Assess the morphology of the erythrocytes.
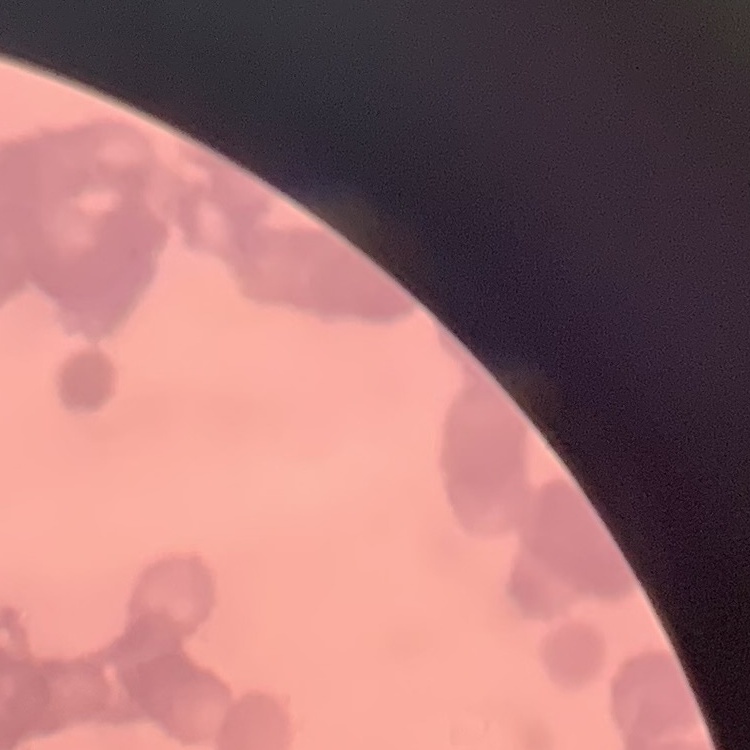
Rouleaux formation.

One tile cut from a larger photomicrograph. Thin peripheral smear. Stained with either Field's or Giemsa.